Outline each Plasmodium ovale-infected red blood cell.
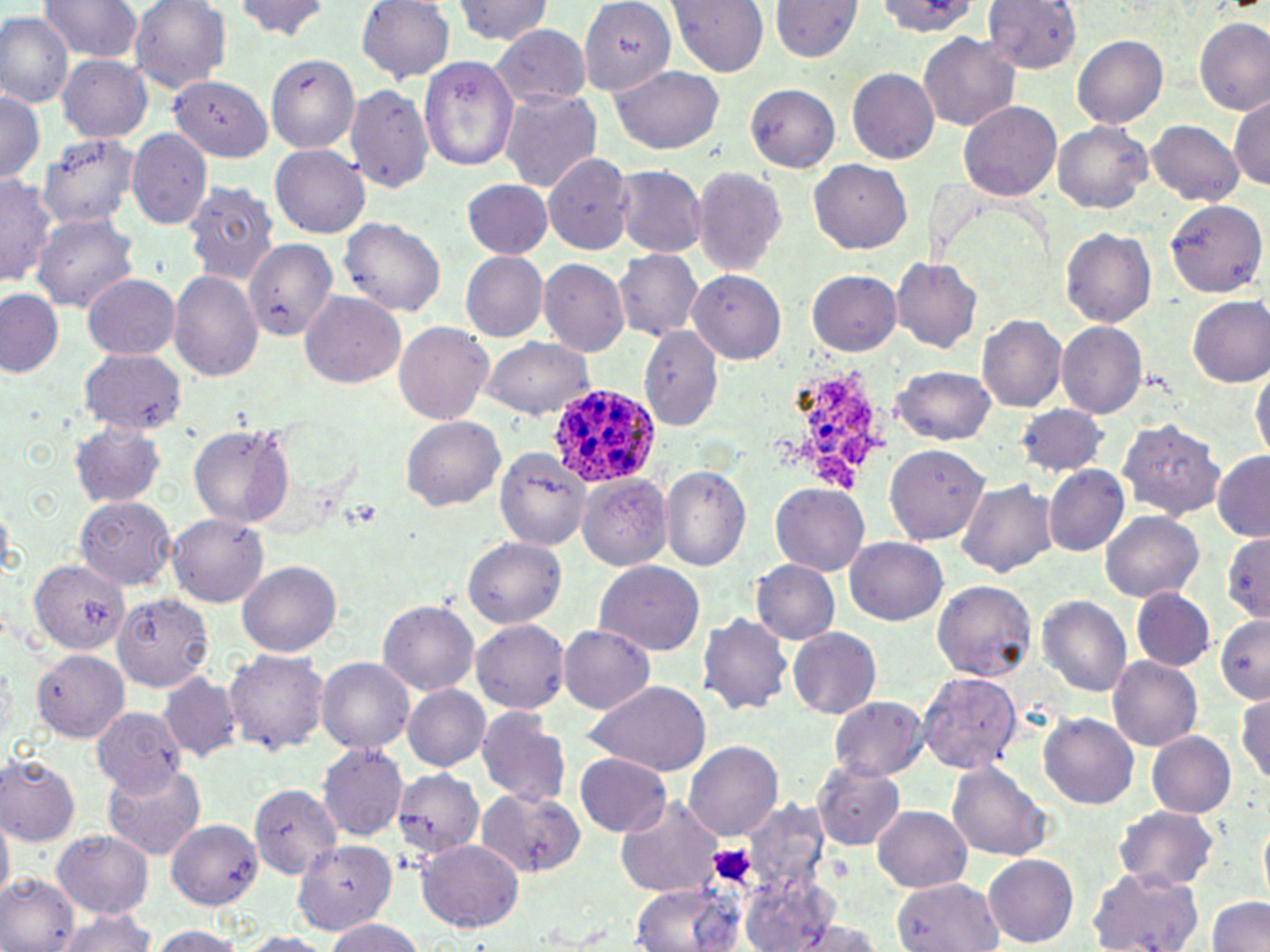

Approximate bounding boxes as (x1, y1, x2, y2) in pixels.
Plasmodium ovale-infected red blood cells: (546, 382, 665, 490).

Summary:
  - Platelet locations: (710, 844, 755, 887)
  - Uninfected red blood cell locations: (129, 0, 231, 91), (234, 0, 332, 42), (580, 0, 677, 97), (669, 0, 769, 75), (871, 0, 978, 39), (982, 0, 1084, 73), (38, 1, 141, 62), (356, 1, 454, 82), (453, 1, 550, 45), (769, 1, 862, 62), (0, 12, 74, 107), (1194, 16, 1269, 115), (489, 24, 593, 109), (918, 32, 1020, 131), (1073, 35, 1168, 128), (263, 53, 360, 154), (56, 55, 153, 141), (417, 55, 519, 172), (608, 64, 724, 154), (847, 68, 940, 164), (368, 71, 497, 193), (169, 74, 274, 161), (344, 83, 435, 194), (744, 83, 841, 172), (0, 88, 45, 186), (498, 88, 602, 192), (1231, 94, 1270, 190), (958, 100, 1061, 201), (1147, 120, 1243, 206), (1052, 121, 1153, 214), (126, 128, 213, 230), (34, 133, 141, 230), (269, 144, 371, 238), (541, 150, 635, 254), (808, 159, 913, 254), (612, 164, 707, 257), (691, 165, 789, 274), (0, 173, 55, 287), (459, 179, 552, 260), (182, 180, 281, 284), (1165, 198, 1269, 296), (33, 214, 138, 309), (337, 216, 445, 316), (1060, 227, 1156, 327), (245, 236, 341, 341), (612, 249, 704, 340), (460, 251, 549, 341), (891, 257, 982, 353), (538, 258, 630, 357), (688, 269, 787, 363), (806, 269, 900, 356), (168, 271, 263, 381), (81, 272, 181, 360), (1, 289, 64, 378), (300, 290, 406, 389), (1187, 294, 1270, 385), (976, 312, 1067, 412), (393, 321, 494, 425), (1055, 321, 1149, 418), (639, 325, 724, 431), (481, 336, 595, 419), (78, 349, 188, 433), (891, 364, 995, 445), (1250, 365, 1270, 463), (1015, 404, 1109, 476), (401, 416, 505, 511), (1119, 418, 1223, 520), (71, 419, 165, 507), (189, 425, 294, 528), (884, 444, 989, 546), (493, 445, 591, 549), (1211, 451, 1270, 542), (659, 466, 750, 570), (1044, 466, 1130, 556), (577, 472, 672, 571), (956, 477, 1059, 579), (771, 484, 868, 575), (74, 495, 179, 589), (1099, 511, 1206, 603), (168, 512, 268, 607), (1221, 532, 1270, 622), (844, 536, 946, 624), (463, 537, 567, 628), (593, 559, 705, 656), (31, 560, 130, 656), (237, 560, 342, 657), (751, 560, 840, 644), (932, 579, 1037, 681), (1131, 587, 1214, 670), (114, 592, 215, 692), (1038, 595, 1132, 695), (377, 598, 479, 694), (696, 614, 793, 715), (1215, 614, 1270, 704), (471, 619, 570, 712), (557, 625, 657, 713), (787, 627, 883, 719), (34, 648, 130, 741), (224, 649, 329, 754), (1107, 655, 1203, 751), (315, 657, 416, 753), (158, 670, 244, 764), (918, 671, 1023, 775), (581, 679, 713, 776), (403, 684, 491, 771), (1233, 688, 1270, 789), (830, 696, 928, 780), (91, 705, 185, 793), (475, 707, 571, 808), (1038, 712, 1138, 809), (1147, 730, 1236, 817), (684, 738, 784, 842), (317, 743, 409, 841), (575, 753, 673, 837), (0, 754, 81, 847), (101, 761, 206, 860), (813, 761, 905, 851), (948, 763, 1053, 861), (393, 767, 486, 858), (249, 784, 344, 878), (476, 788, 587, 879), (617, 795, 727, 897), (1113, 805, 1220, 891), (870, 806, 972, 893), (0, 811, 14, 902), (1257, 816, 1269, 910), (165, 819, 264, 909), (53, 830, 154, 919), (417, 837, 523, 932), (291, 840, 397, 932), (981, 853, 1079, 946), (1087, 868, 1206, 952), (734, 870, 845, 952), (0, 873, 78, 950), (894, 877, 1003, 952), (624, 881, 745, 952), (1205, 896, 1270, 951), (52, 909, 158, 951), (773, 917, 890, 952), (321, 918, 427, 952), (145, 925, 248, 951), (236, 932, 334, 951)
  - Slide-level diagnosis: Plasmodium ovale
  - Preparation: thin blood film
  - Magnification: 1000x
  - Field of view: one of a larger specimen
  - Image size: 1270×952 pixels
  - Modality: light microscopy
  - Stain: May-Grünwald-Giemsa